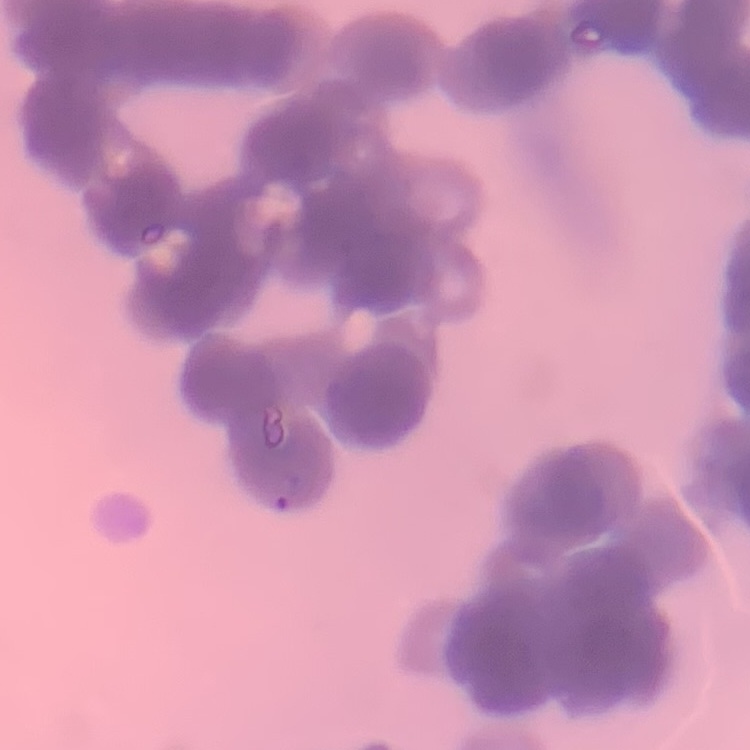 The red blood cells show rouleaux formation. Square crop of a larger photomicrograph. Stained with either Field's or Giemsa. Thin blood smear.